Assess this cell for malaria.
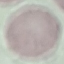

It is uninfected.

Summary:
  - Stain: Giemsa
  - Capture: smartphone camera at the microscope eyepiece
  - Image type: cell patch, automatically extracted from a larger field of view and resized to 64 × 64 pixels
  - Preparation: thin smear